State which parasite is depicted.
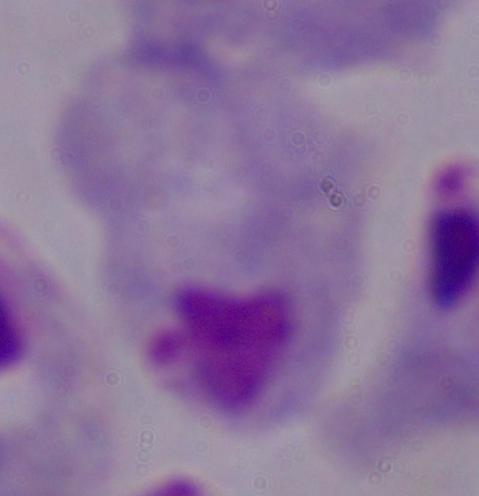
A trichomonad.

modality = photomicrograph
magnification = 1000x